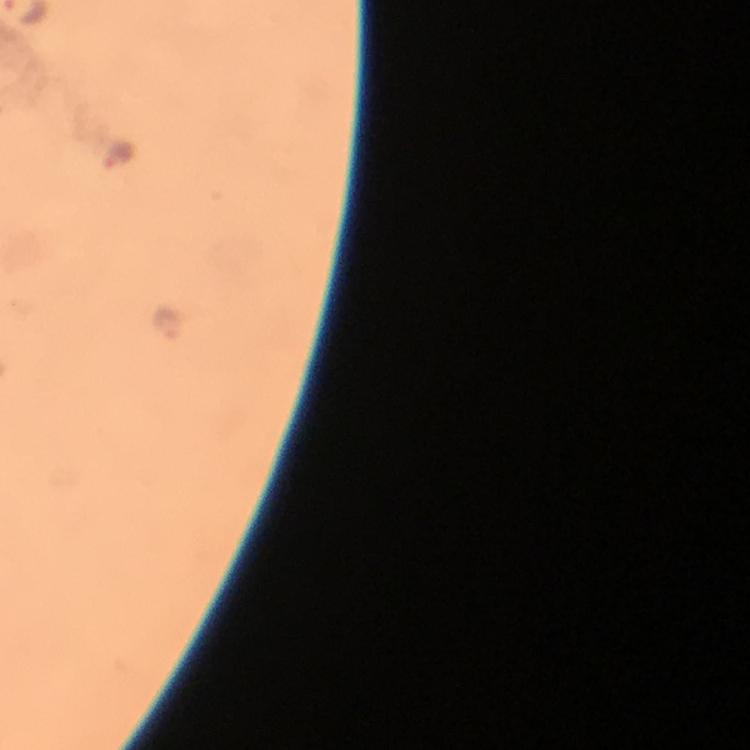

{
  "preparation": "thick blood smear",
  "immersion_oil": "applied",
  "malaria_parasite_locations": "approximate centers as {x, y} in pixels: {118, 154}, {174, 327}",
  "context": "from a malaria diagnostic workup",
  "stain": "Giemsa",
  "cropped_from": "one field of view",
  "image_size": "750×750 pixels",
  "magnification": "100x",
  "capture": "smartphone mounted on the microscope"
}